Evaluate for malaria.
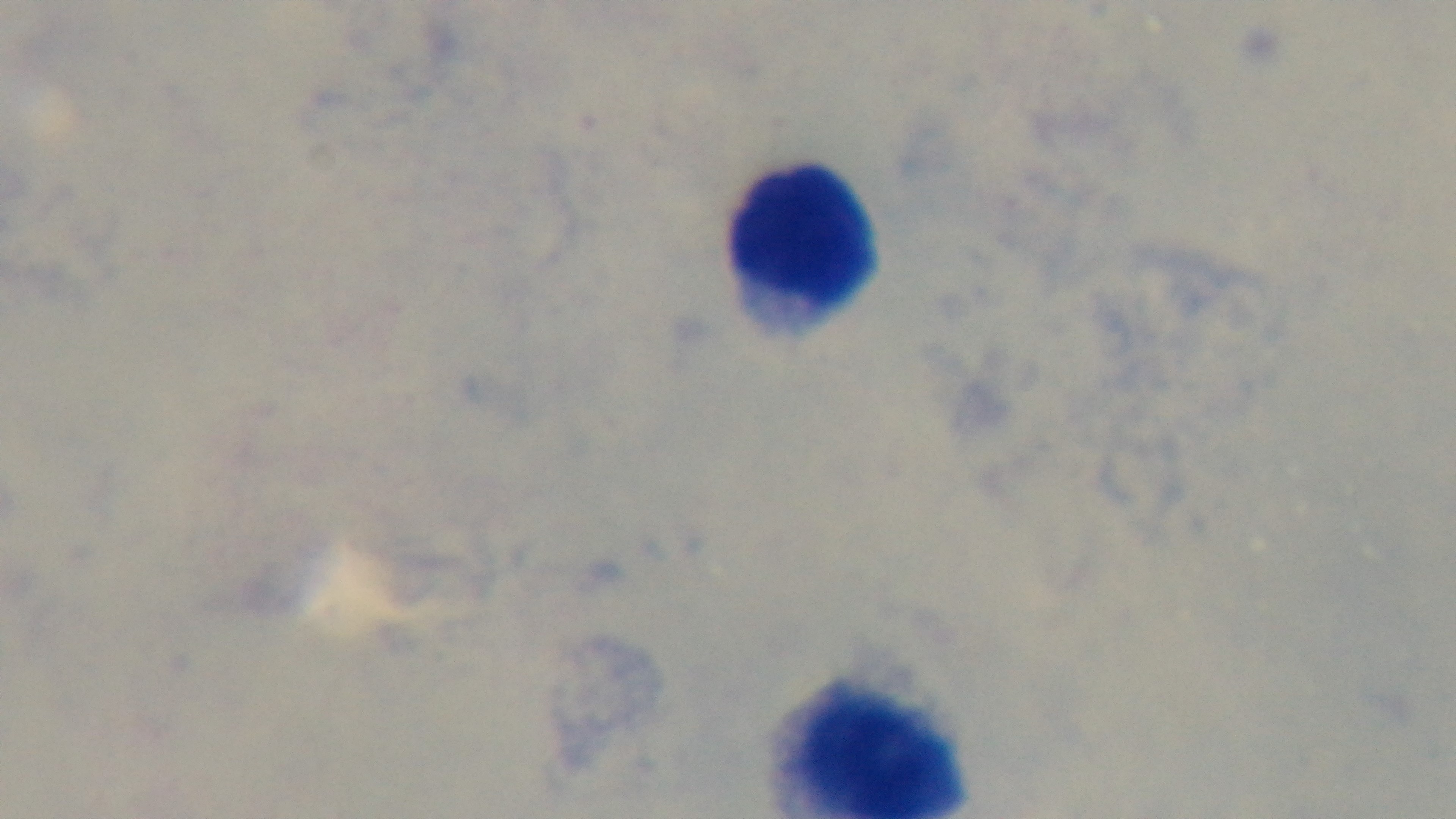
Uninfected.

Preparation: thick. Giemsa-stained. Captured with a mounted 4K digital camera. Oil-immersion objective, 100x. Light microscopy. One field from the slide.